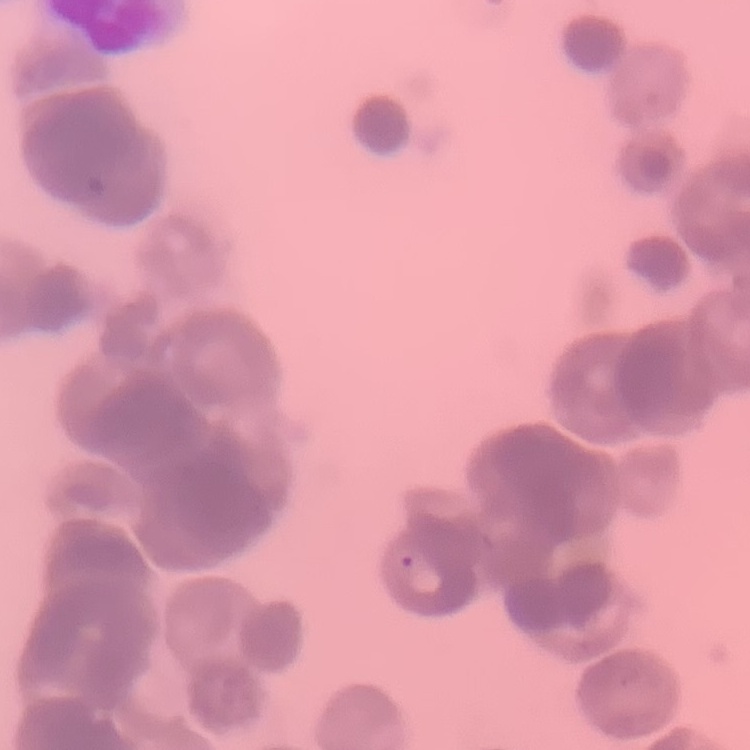
erythrocyte_morphology: rouleaux formation
image_type: square crop of a larger photomicrograph
preparation: thin blood film
stain: Field's or Giemsa